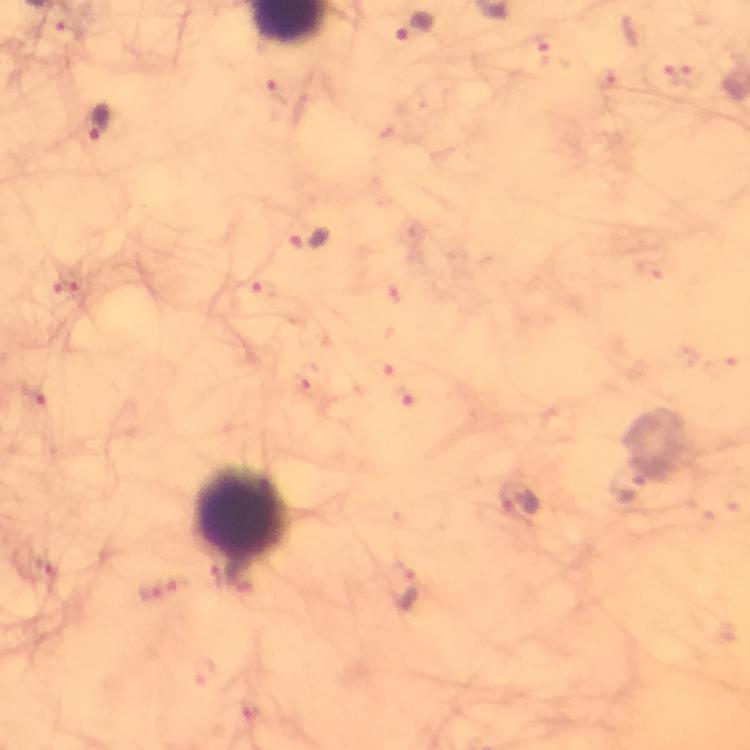
Approximate object centers, in pixels from the top-left corner. Leukocyte locations: (x=241, y=520). Malaria parasite locations: (x=418, y=29), (x=99, y=124), (x=310, y=240), (x=519, y=501), (x=403, y=586). Image is 750×750 pixels. Smartphone photograph taken through a microscope. Giemsa-stained preparation. Cropped region of a single field of view. Thick smear. From a diagnostic examination for malaria. Immersion oil was used. At 100x magnification.